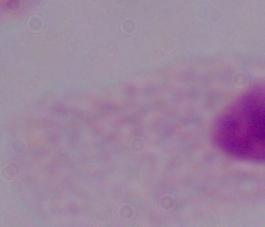
Summary:
  - Magnification: 1000x
  - Modality: photomicrograph
  - Identification: trichomonad